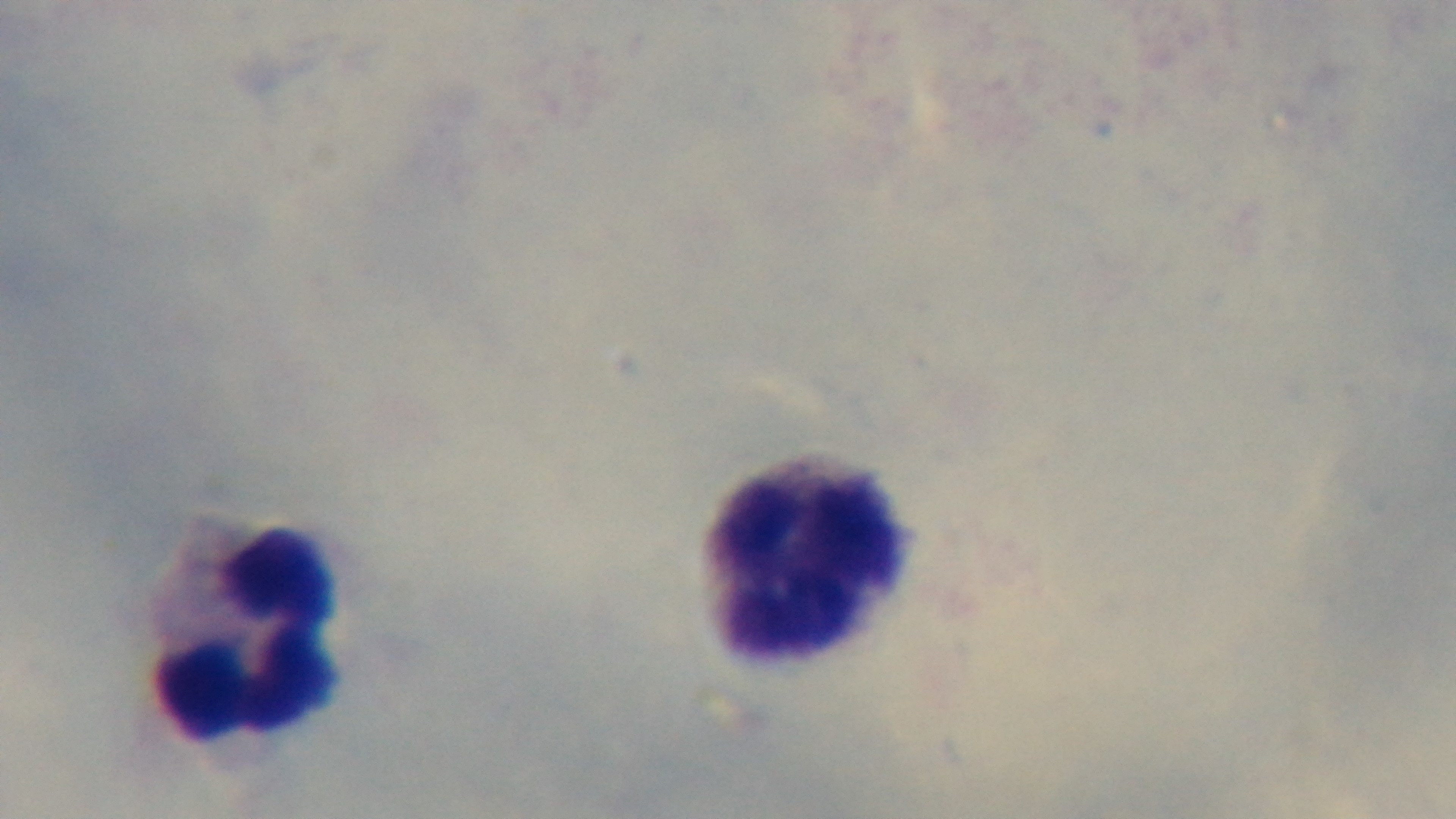
Summary:
  - Objective: 100x oil immersion
  - Modality: light microscopy
  - Malaria status: uninfected
  - Preparation: thick
  - Field of view: one from the slide
  - Capture: mounted 4K digital camera
  - Stain: Giemsa